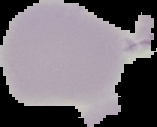

Result: no Plasmodium parasites seen. Image is 157×127 pixels. Segmented cell region on a black background. From a thin blood film.